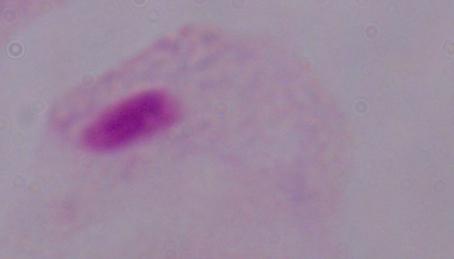
Summary:
  - Modality: photomicrograph
  - Magnification: 1000x
  - Identification: trichomonad